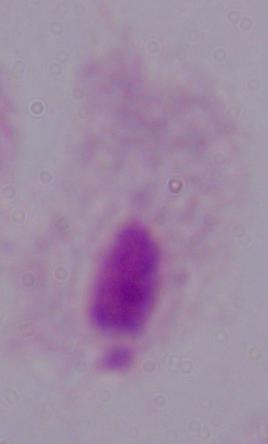

Summary:
  - Magnification: 1000x
  - Identification: trichomonad
  - Modality: micrograph